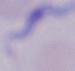
modality = micrograph
magnification = 1000x
identification = trypanosome